Describe the morphology of the red blood cells.
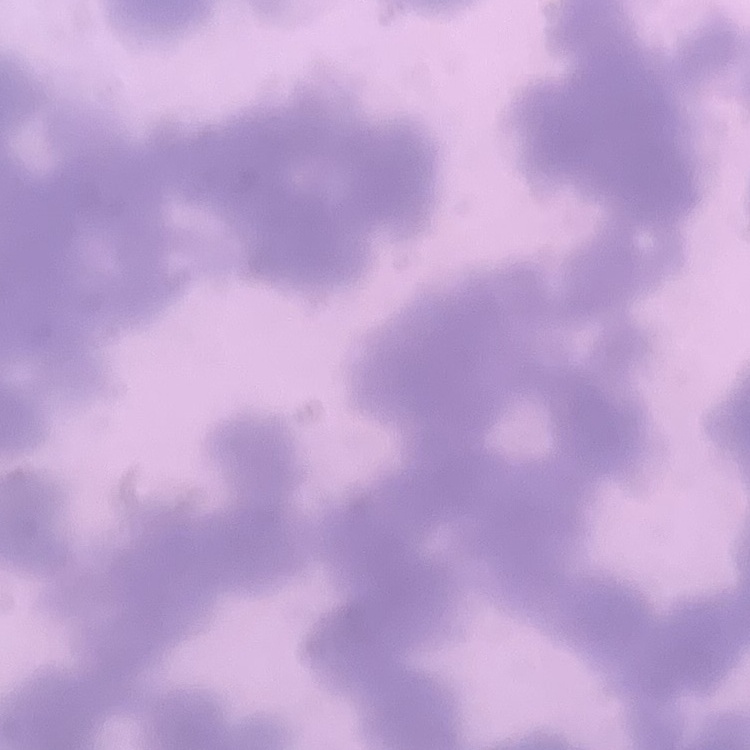

Rouleaux formation.

Thin blood film. Square crop of a larger photomicrograph. Field's or Giemsa stain.